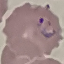
malaria_status: parasitized
preparation: thin smear
capture: smartphone through the microscope eyepiece
stain: Giemsa
image_type: automatically extracted cell patch, resized to 64 × 64 pixels